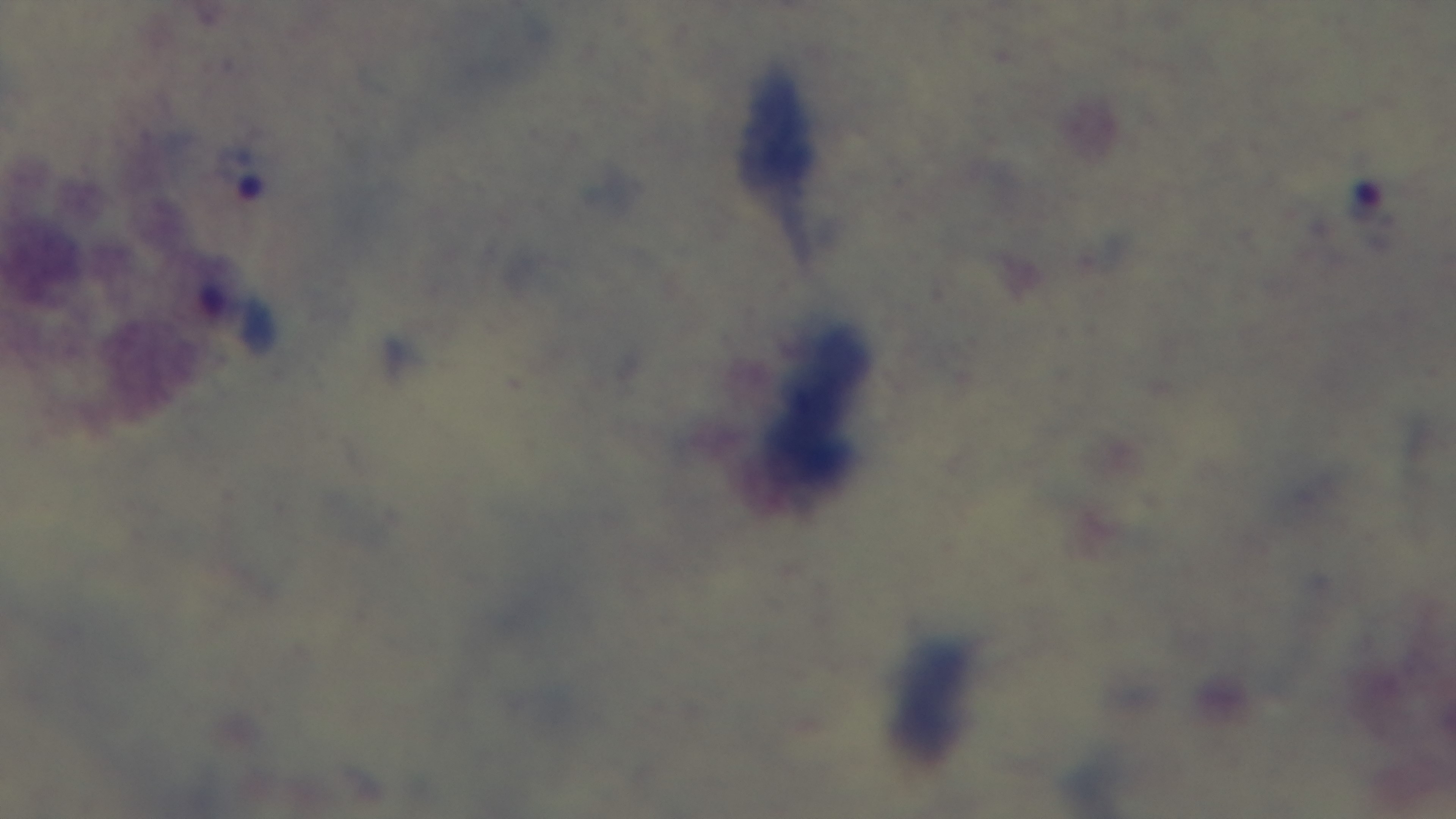

objective: 100x oil immersion
malaria_status: positive
field_of_view: single
modality: light microscopy
stain: Giemsa
preparation: thick
capture: mounted 4K digital camera